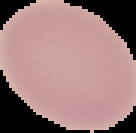

Segmented cell region on a black background. From a thin blood smear. Image is 136×133 pixels. Malaria status: uninfected.